Report the malaria status.
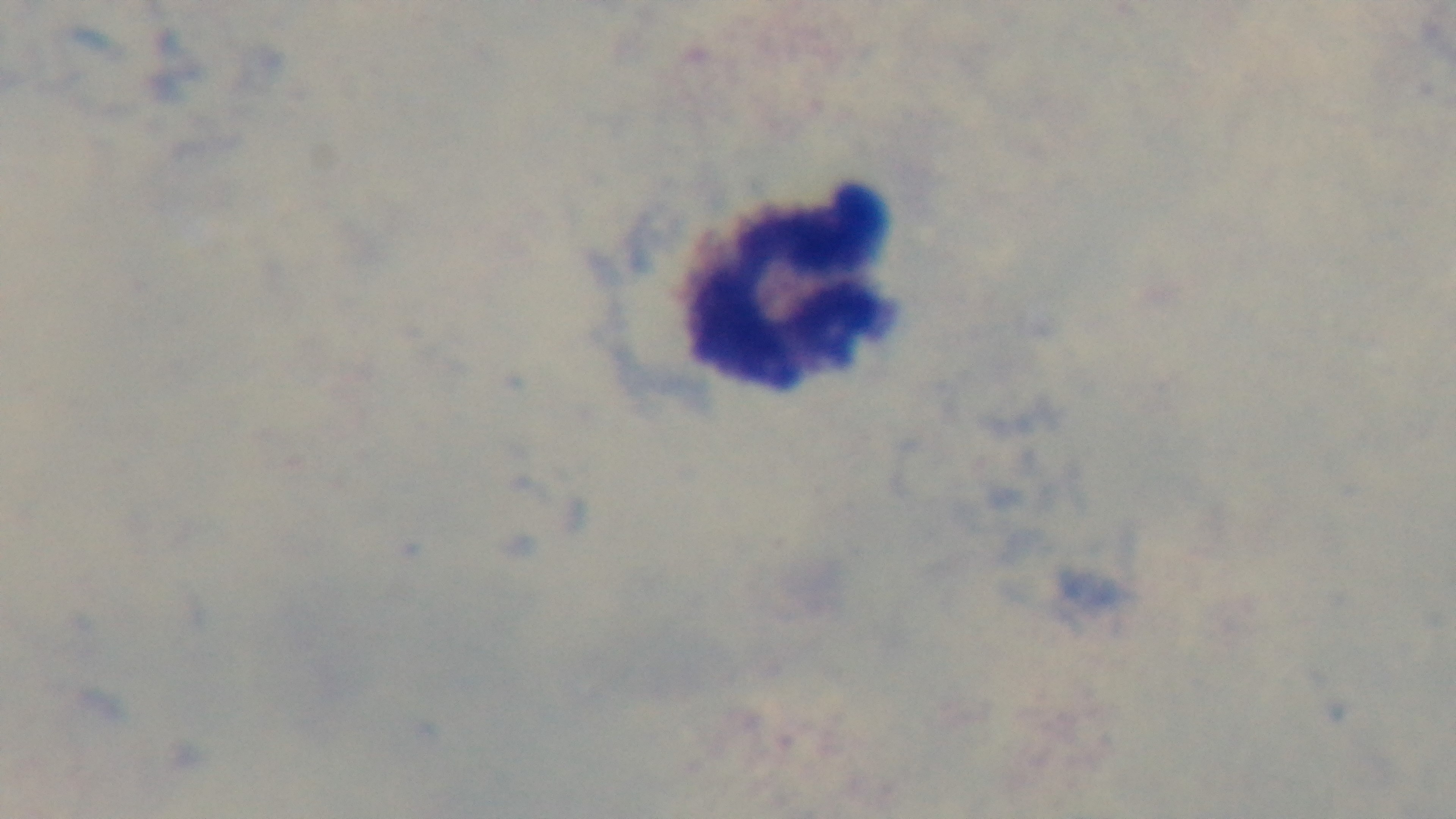

Uninfected.

stain = Giemsa
field of view = one from the slide
preparation = thick blood film
objective = 100x oil immersion
capture = mounted 4K digital camera
modality = light microscopy